Locate every Plasmodium parasite.
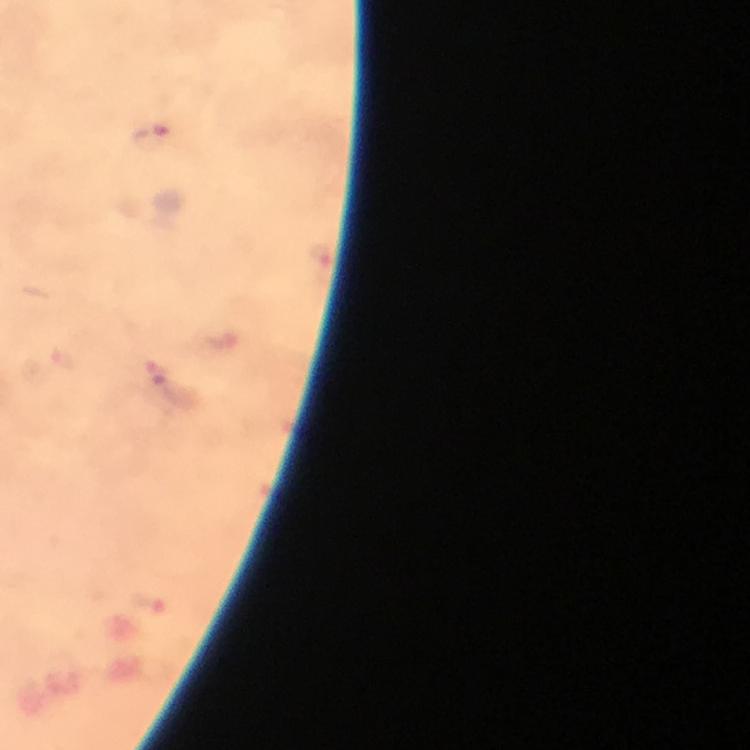

Approximate object centers, in pixels from the top-left corner.
Plasmodium parasites: (x=153, y=139).

context = from a diagnostic examination for malaria
cropped from = one field of view
magnification = 100x
immersion oil = applied
preparation = thick blood smear
stain = Giemsa
capture = smartphone mounted on the microscope
image size = 750×750 pixels